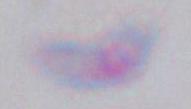
{
  "modality": "photomicrograph",
  "magnification": "1000x",
  "identification": "Toxoplasma gondii"
}